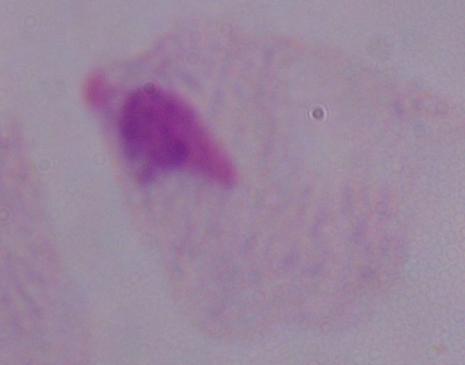
Summary:
  - Modality: photomicrograph
  - Magnification: 1000x
  - Identification: trichomonad